Assess this cell for malaria.
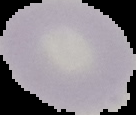

It is uninfected.

{
  "image_size": "136×115 pixels",
  "preparation": "thin blood film",
  "image_type": "segmented cell region with the area outside set to black"
}